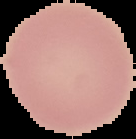

Summary:
  - Image size: 136×139 pixels
  - Image type: segmented cell region with the area outside set to black
  - Preparation: thin blood smear
  - Result: negative for malaria parasites